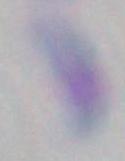
Summary:
  - Identification: Toxoplasma gondii
  - Magnification: 1000x
  - Modality: photomicrograph